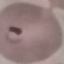
result = malaria parasites identified
capture = smartphone camera at the microscope eyepiece
stain = Giemsa
image type = automatically extracted cell patch, resized to 64 × 64 pixels
preparation = thin blood smear